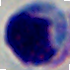

A white blood cell is seen. Captured at 1000x magnification. Photomicrograph.